Report the malaria status of this cell.
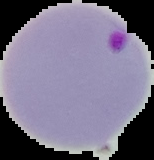

It is parasitized.

{
  "image_type": "segmented cell region with the area outside set to black",
  "image_size": "154×160 pixels",
  "preparation": "thin blood smear"
}